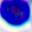

Summary:
  - Modality: micrograph
  - Identification: leukocyte
  - Magnification: 400x